Outline each blood parasite and name the species.
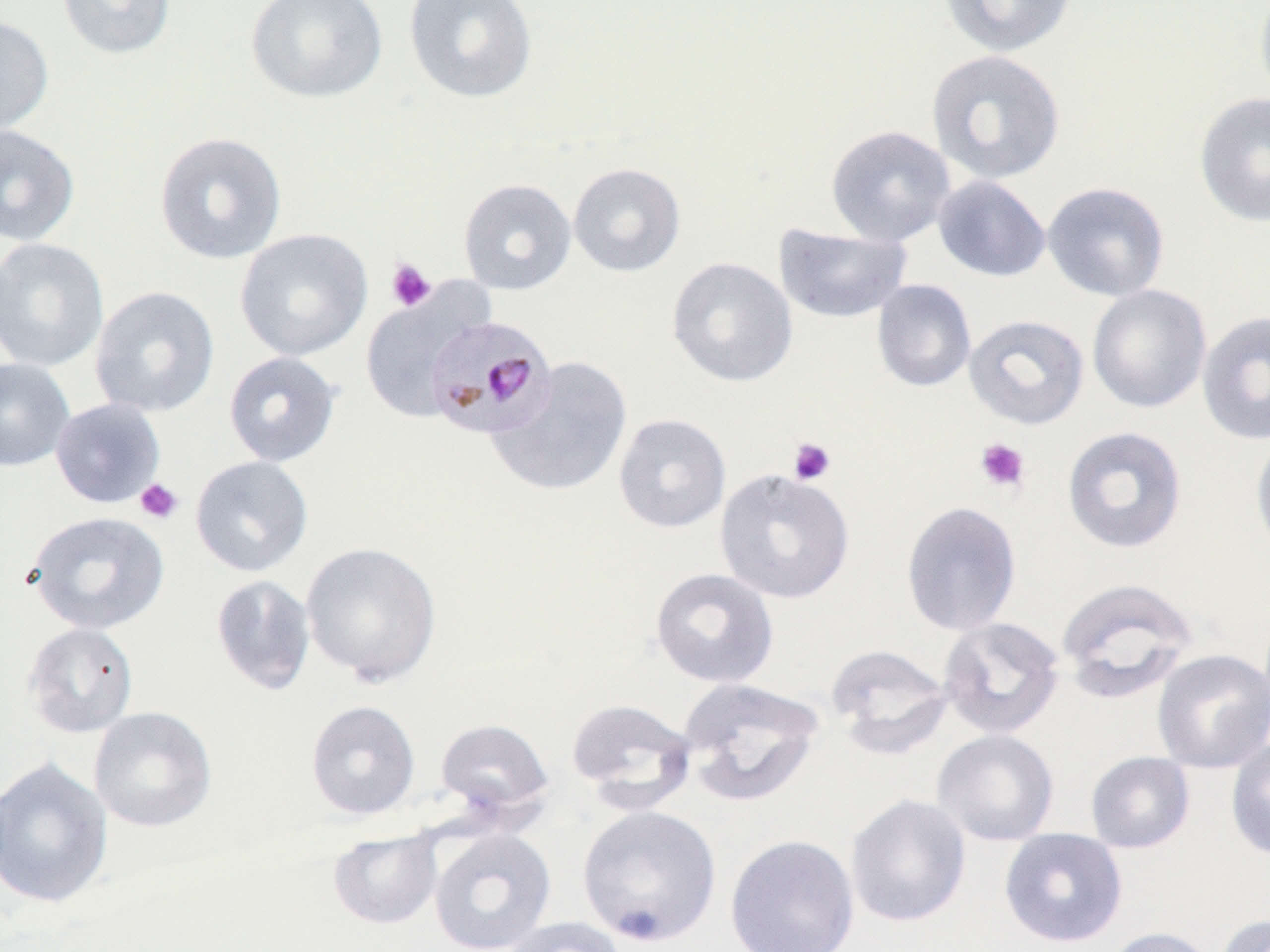

Approximate bounding boxes as [x1, y1, x2, y2] in pixels.
Plasmodium malariae-infected red blood cells: [424, 315, 557, 440].
No Plasmodium falciparum, Plasmodium ovale, Plasmodium vivax, Babesia divergens, or Trypanosoma brucei observed.

Platelet locations: [386, 258, 437, 312], [787, 437, 836, 485], [975, 437, 1030, 493], [135, 478, 184, 524]. Uninfected red blood cell locations: [56, 0, 176, 60], [246, 0, 388, 103], [403, 0, 538, 103], [939, 0, 1078, 57], [1254, 0, 1270, 105], [0, 14, 54, 139], [926, 49, 1066, 185], [1194, 91, 1270, 229], [0, 123, 80, 246], [826, 124, 956, 247], [154, 131, 287, 264], [568, 162, 685, 277], [932, 175, 1051, 282], [458, 178, 577, 295], [1041, 181, 1170, 302], [774, 223, 912, 324], [234, 228, 373, 361], [0, 237, 110, 372], [666, 256, 798, 387], [872, 279, 976, 392], [1087, 284, 1212, 413], [90, 285, 220, 417], [360, 288, 485, 423], [1197, 310, 1270, 446], [963, 314, 1089, 429], [223, 351, 342, 467], [487, 356, 634, 497], [0, 357, 76, 472], [50, 397, 166, 509], [613, 413, 731, 533], [1061, 425, 1188, 554], [1250, 432, 1270, 560], [190, 455, 313, 576], [714, 467, 855, 604], [901, 501, 1022, 636], [25, 511, 170, 634], [301, 541, 442, 686], [650, 567, 779, 688], [211, 575, 316, 695], [1056, 577, 1200, 703], [938, 616, 1065, 739], [22, 622, 139, 738], [825, 644, 954, 758], [1152, 649, 1270, 773], [678, 677, 825, 807], [566, 697, 698, 812], [305, 700, 421, 819], [88, 706, 218, 832], [436, 718, 554, 818], [932, 729, 1059, 846], [1225, 737, 1270, 860], [1086, 751, 1195, 853], [0, 756, 113, 909], [845, 793, 972, 928], [577, 804, 722, 945], [428, 828, 556, 952], [999, 828, 1128, 948], [328, 829, 443, 929], [725, 834, 860, 952], [1215, 913, 1270, 952], [501, 917, 627, 952], [1101, 926, 1220, 952]. Slide-level diagnosis: Plasmodium malariae. Image is 1270×952 pixels. Thin blood film. One field of a larger specimen. Optical microscopy. Captured at 1000x magnification. May-Grünwald-Giemsa stain.